Mark where platelets are.
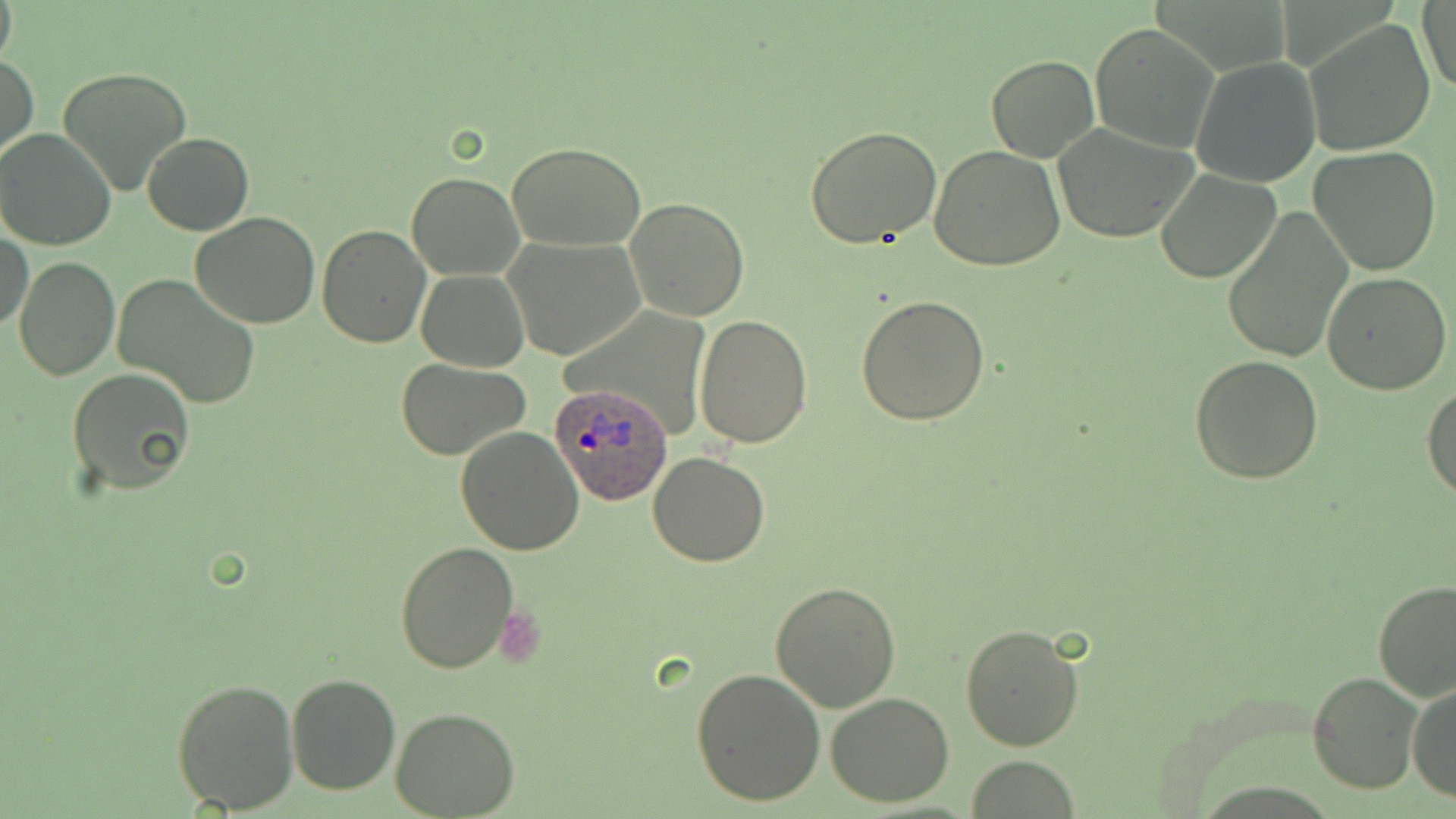
Approximate bounding boxes as named x1/y1/x2/y2 corners in pixels.
Platelets: (x1=498, y1=609, x2=546, y2=667).

Plasmodium ovale-infected red blood cell locations: (x1=548, y1=380, x2=675, y2=506). Uninfected red blood cell locations: (x1=0, y1=0, x2=17, y2=71), (x1=1417, y1=3, x2=1455, y2=93), (x1=1303, y1=18, x2=1438, y2=156), (x1=1089, y1=23, x2=1219, y2=153), (x1=1, y1=54, x2=37, y2=164), (x1=985, y1=54, x2=1100, y2=163), (x1=1190, y1=55, x2=1322, y2=189), (x1=58, y1=65, x2=194, y2=196), (x1=1050, y1=122, x2=1202, y2=242), (x1=805, y1=124, x2=942, y2=247), (x1=0, y1=129, x2=116, y2=251), (x1=142, y1=132, x2=253, y2=235), (x1=505, y1=142, x2=648, y2=252), (x1=929, y1=145, x2=1065, y2=270), (x1=1308, y1=147, x2=1442, y2=278), (x1=1157, y1=169, x2=1282, y2=283), (x1=407, y1=171, x2=524, y2=280), (x1=623, y1=198, x2=749, y2=322), (x1=1222, y1=209, x2=1351, y2=365), (x1=190, y1=213, x2=322, y2=329), (x1=317, y1=225, x2=431, y2=348), (x1=1, y1=228, x2=32, y2=335), (x1=503, y1=235, x2=646, y2=361), (x1=12, y1=256, x2=119, y2=381), (x1=417, y1=270, x2=528, y2=372), (x1=1323, y1=272, x2=1453, y2=394), (x1=114, y1=276, x2=261, y2=406), (x1=858, y1=296, x2=991, y2=426), (x1=694, y1=316, x2=812, y2=448), (x1=1191, y1=354, x2=1324, y2=484), (x1=396, y1=359, x2=531, y2=459), (x1=67, y1=368, x2=197, y2=498), (x1=1423, y1=385, x2=1456, y2=501), (x1=455, y1=428, x2=584, y2=555), (x1=648, y1=453, x2=771, y2=567), (x1=394, y1=540, x2=521, y2=672), (x1=1373, y1=579, x2=1455, y2=701), (x1=768, y1=581, x2=901, y2=712), (x1=960, y1=624, x2=1085, y2=751), (x1=690, y1=666, x2=826, y2=807), (x1=1308, y1=671, x2=1423, y2=795), (x1=286, y1=674, x2=399, y2=795), (x1=171, y1=676, x2=300, y2=814), (x1=1408, y1=683, x2=1455, y2=804), (x1=826, y1=692, x2=955, y2=807), (x1=392, y1=708, x2=520, y2=818), (x1=967, y1=755, x2=1080, y2=818). Slide-level diagnosis: Plasmodium ovale. Optical microscopy. May-Grünwald-Giemsa-stained preparation. Image is 1456×819 pixels. One field of a larger specimen. Thin blood film. Captured at 1000x magnification.